Classify this cell by malaria status.
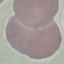
Uninfected.

image type = automatically extracted cell patch, resized to 64 × 64 pixels
capture = smartphone through the microscope eyepiece
preparation = thin blood film
stain = Giemsa